Comment on the morphology of the red blood cells.
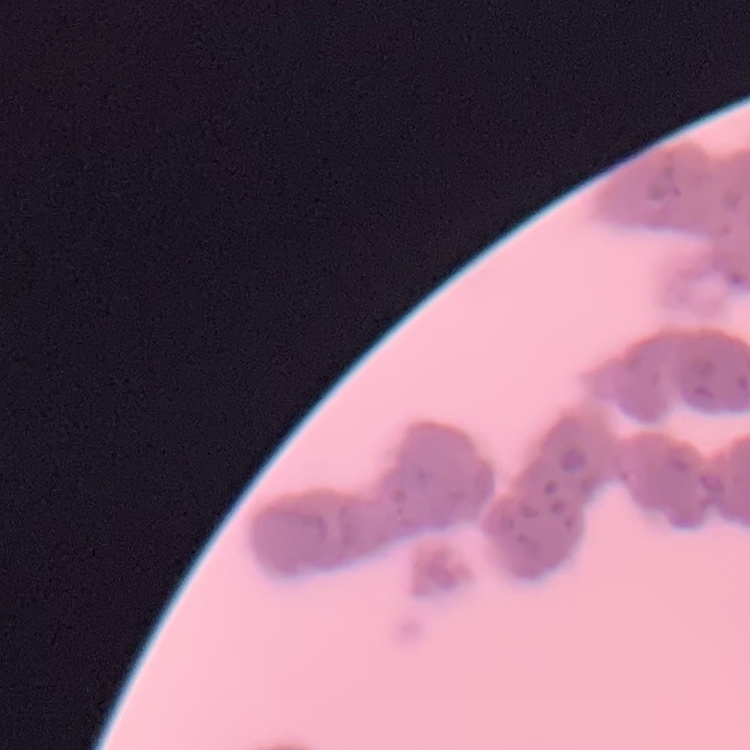
They show rouleaux formation.

Summary:
  - Image type: one tile cut from a larger photomicrograph
  - Stain: Field's or Giemsa
  - Preparation: thin blood smear